Outline each uninfected red blood cell.
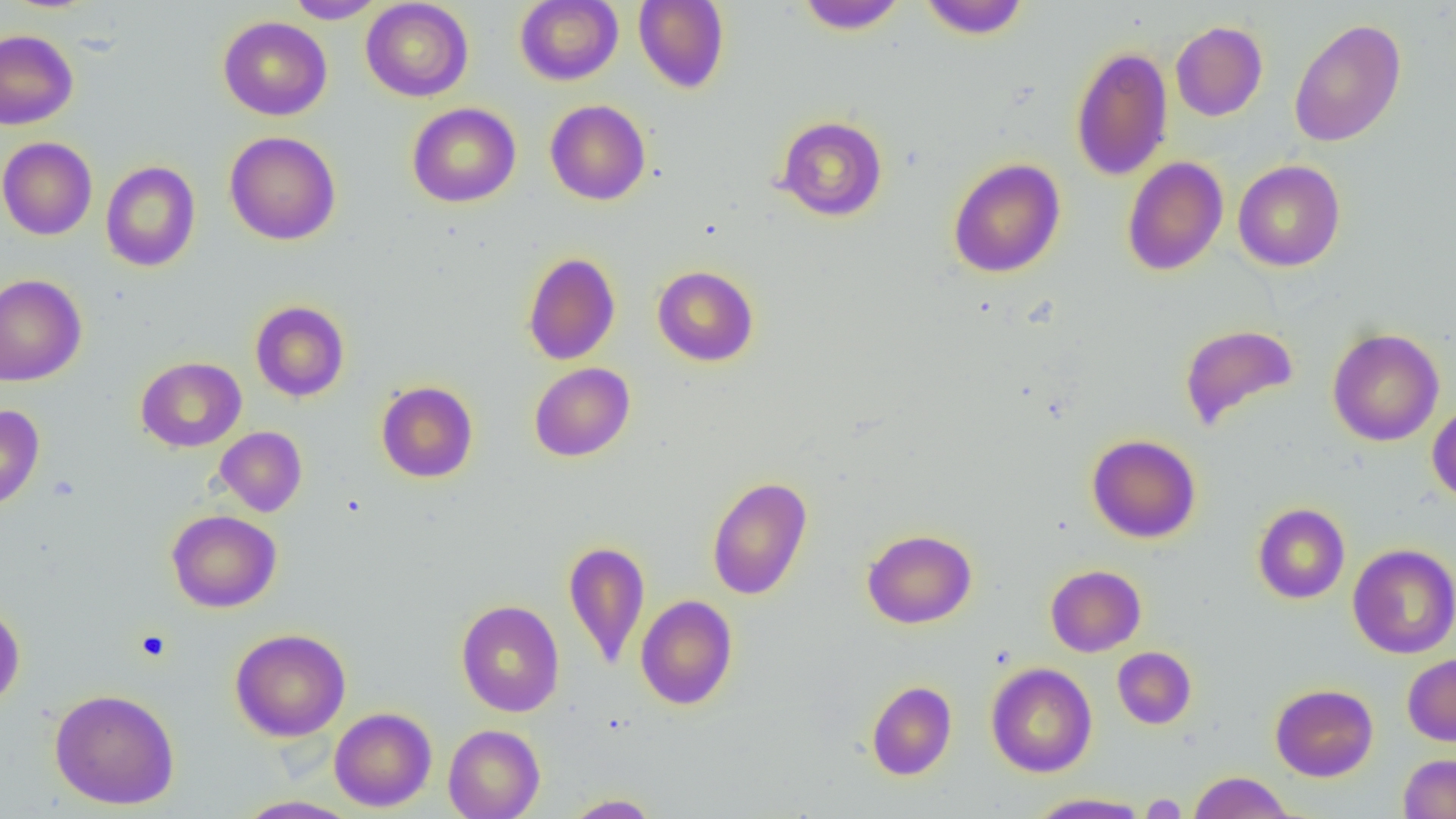
Approximate bounding boxes as [x1, y1, x2, y2] in pixels.
Uninfected red blood cells: [285, 0, 386, 23], [514, 0, 623, 86], [634, 0, 729, 93], [795, 0, 908, 34], [918, 0, 1030, 39], [360, 1, 473, 101], [218, 16, 332, 121], [1288, 18, 1406, 147], [1171, 20, 1268, 121], [0, 29, 78, 130], [1070, 45, 1173, 182], [545, 100, 651, 205], [407, 102, 521, 207], [776, 115, 888, 221], [224, 131, 341, 245], [0, 137, 98, 240], [1122, 157, 1228, 276], [948, 158, 1066, 278], [1233, 159, 1345, 272], [100, 160, 201, 272], [522, 251, 620, 365], [652, 265, 759, 366], [0, 274, 86, 386], [250, 300, 350, 401], [1179, 324, 1300, 432], [1327, 328, 1444, 447], [135, 356, 246, 452], [529, 362, 635, 462], [376, 381, 478, 483], [1427, 403, 1456, 504], [0, 404, 45, 511], [215, 426, 307, 516], [1087, 434, 1201, 543], [707, 476, 813, 601], [1252, 503, 1350, 604], [167, 510, 282, 612], [862, 528, 977, 629], [563, 540, 650, 670], [1348, 543, 1456, 658], [1045, 565, 1146, 656], [636, 594, 738, 710], [456, 599, 565, 717], [0, 604, 25, 710], [230, 628, 351, 741], [1112, 647, 1196, 729], [1402, 653, 1456, 746], [986, 662, 1097, 777], [866, 680, 956, 780], [1270, 683, 1378, 781], [49, 687, 180, 810], [329, 707, 437, 812], [443, 724, 545, 819], [1398, 753, 1456, 818], [1188, 771, 1295, 818], [1027, 792, 1151, 818], [563, 794, 661, 818], [233, 795, 361, 818].

Summary:
  - Platelet locations: [133, 628, 171, 662], [1140, 794, 1188, 817]
  - Slide-level diagnosis: negative for blood parasites
  - Preparation: thin blood smear
  - Image size: 1456×819 pixels
  - Modality: optical microscopy
  - Field of view: one of a larger specimen
  - Magnification: 1000x